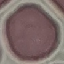
result = no malaria parasites seen
capture = smartphone camera at the microscope eyepiece
stain = Giemsa
image type = automatically extracted cell patch, resized to 64 × 64 pixels
preparation = thin smear